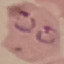

{
  "malaria_status": "parasitized",
  "stain": "Giemsa",
  "preparation": "thin smear",
  "capture": "smartphone camera at the microscope eyepiece",
  "image_type": "cell patch, automatically extracted from a larger field of view and resized to 64 × 64 pixels"
}